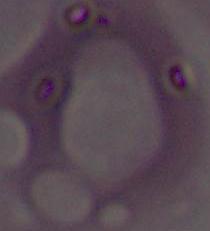
Summary:
  - Identification: red blood cell
  - Magnification: 1000x
  - Modality: micrograph